Report the malaria status of this cell.
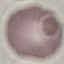

It is uninfected.

Photographed with a smartphone camera at the microscope eyepiece. Cell patch, automatically extracted from a larger field of view and resized to 64 × 64 pixels. Giemsa-stained preparation. Thin blood film.